Describe the morphology of the red blood cells.
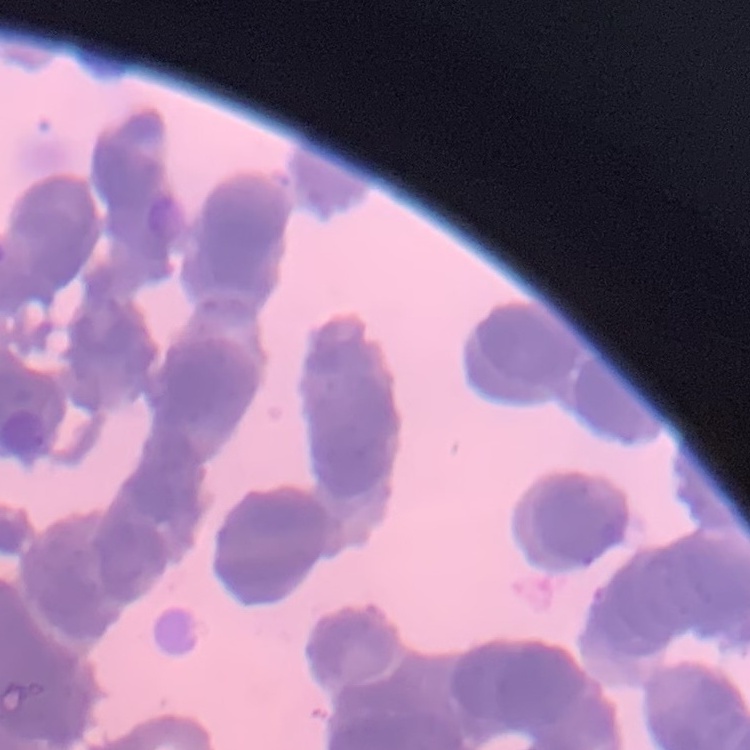
Rouleaux formation.

Summary:
  - Image type: one tile cut from a larger photomicrograph
  - Preparation: thin blood film
  - Stain: Field's or Giemsa